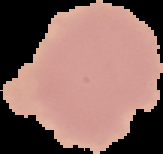

{
  "result": "negative for Plasmodium parasites",
  "image_type": "segmented cell region on a black background",
  "preparation": "thin blood smear",
  "image_size": "163×154 pixels"
}